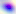

Summary:
  - Identification: Toxoplasma gondii
  - Magnification: 400x
  - Modality: micrograph